Report the malaria status of this cell.
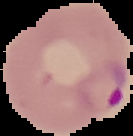

It is parasitized.

Segmented cell region on a black background. Image is 133×136 pixels. From a thin blood film.